Locate platelets.
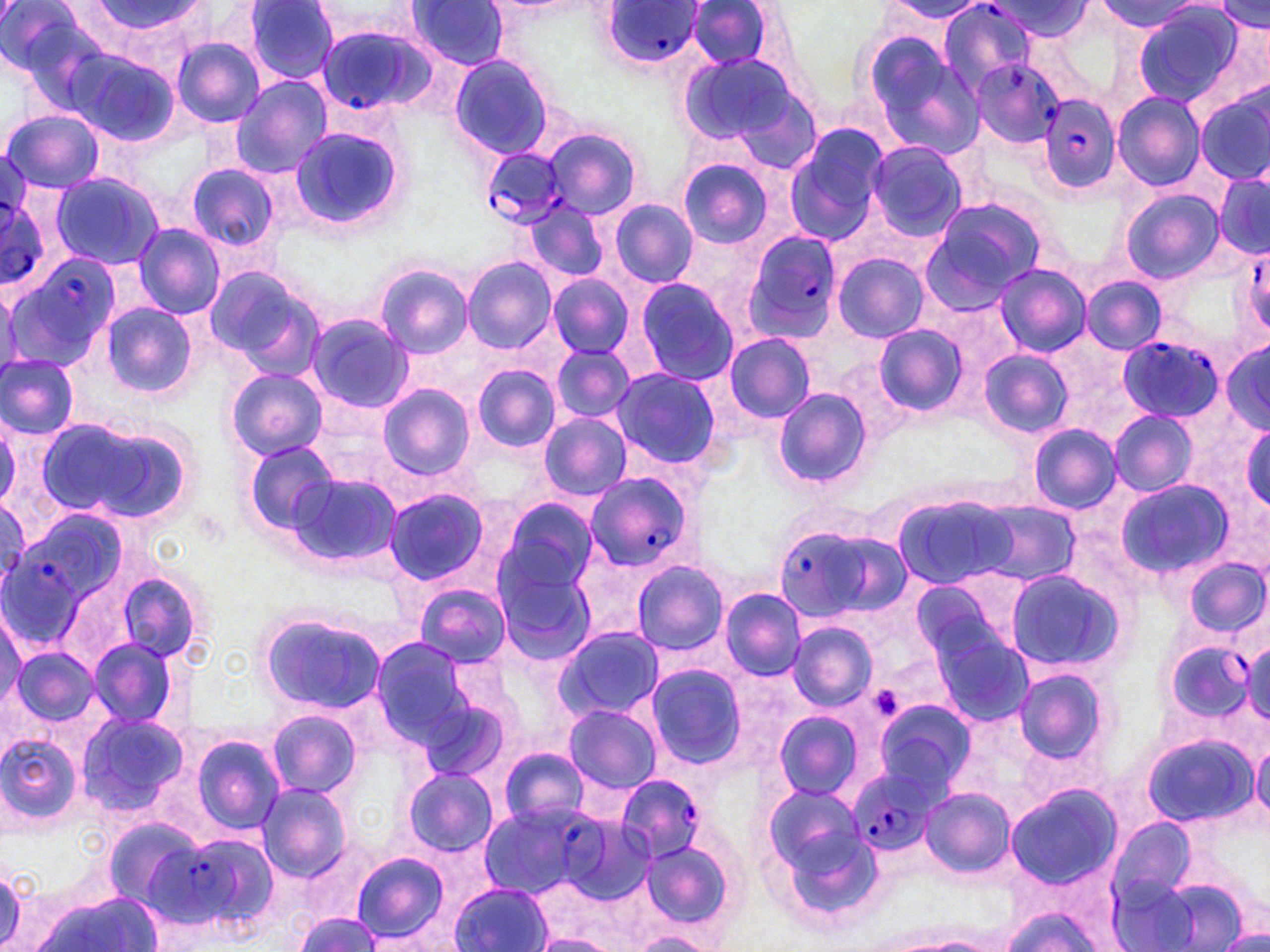

Approximate bounding boxes as (x1,y1)-(x2,y2) corner pairs in pixels.
Platelets: (868,683)-(907,723).

Summary:
  - Plasmodium falciparum-infected red blood cell locations (subset): (940,0)-(1040,91), (599,2)-(704,72), (311,15)-(430,114), (966,58)-(1062,148), (1036,92)-(1121,196), (479,148)-(568,231), (0,193)-(47,283), (740,229)-(846,343), (1251,251)-(1270,328), (7,255)-(124,374), (1117,338)-(1220,422), (583,470)-(699,574), (776,522)-(907,625), (0,536)-(83,646), (1166,636)-(1256,722), (851,768)-(937,857), (614,773)-(706,860), (156,830)-(280,937)
  - Uninfected red blood cell locations (subset): (89,0)-(204,42), (406,0)-(512,69), (1101,0)-(1201,32), (1,1)-(103,101), (243,1)-(340,84), (885,1)-(987,22), (686,2)-(773,70), (989,2)-(1088,41), (306,3)-(423,49), (1215,3)-(1268,34), (1132,5)-(1242,106), (862,35)-(985,157), (171,37)-(264,127), (63,47)-(180,146), (448,54)-(555,161), (679,54)-(806,153), (230,77)-(331,179), (1112,92)-(1206,192), (1197,93)-(1270,184), (2,109)-(104,193), (785,124)-(888,246), (287,126)-(404,232), (542,126)-(642,220), (867,141)-(965,241), (678,158)-(772,247), (185,162)-(279,253), (49,172)-(165,270), (1214,172)-(1270,258), (1120,188)-(1224,282), (918,197)-(1048,308), (609,199)-(699,287), (523,201)-(610,284), (133,225)-(224,319), (834,252)-(927,342), (462,256)-(558,355), (992,262)-(1089,358), (375,264)-(472,357), (201,266)-(319,375), (547,276)-(634,359), (1080,276)-(1167,356), (633,277)-(739,387), (100,304)-(197,399), (306,313)-(412,412), (872,324)-(968,415), (722,333)-(816,423), (1221,339)-(1270,434), (548,344)-(636,424), (979,348)-(1073,438), (0,355)-(78,439), (826,355)-(917,448), (471,364)-(562,452), (610,367)-(727,473), (227,368)-(328,460), (0,370)-(111,485), (377,383)-(476,480), (771,388)-(871,490), (1109,409)-(1198,496), (537,412)-(634,501), (0,413)-(21,511), (37,415)-(181,524), (1028,423)-(1119,513), (1242,423)-(1270,513), (242,439)-(339,533), (287,471)-(402,570), (1114,478)-(1232,579), (383,488)-(490,586), (895,494)-(1018,588), (498,499)-(599,598), (973,500)-(1080,585), (492,554)-(601,672), (1183,557)-(1269,636), (630,559)-(730,656), (1002,568)-(1126,675), (112,570)-(210,667), (909,571)-(1022,670), (413,581)-(509,668), (720,587)-(807,680), (256,608)-(388,715), (1,612)-(26,709), (788,622)-(876,712), (930,625)-(1035,729), (555,627)-(666,722), (370,636)-(477,747), (88,638)-(180,729), (1247,640)-(1270,726), (11,646)-(99,727), (645,663)-(748,769), (1012,665)-(1112,768), (417,696)-(509,788), (872,698)-(975,795), (564,704)-(661,794), (266,708)-(360,799), (773,709)-(864,801), (76,711)-(191,821), (0,731)-(84,832), (190,733)-(285,833), (1141,734)-(1258,828), (1252,741)-(1270,826), (499,747)-(589,829), (402,767)-(498,858), (758,781)-(875,898), (255,784)-(352,882), (1004,785)-(1122,888), (920,788)-(1015,879), (564,816)-(660,904), (100,817)-(205,910), (1106,818)-(1199,922), (640,839)-(734,932), (351,852)-(450,944), (0,865)-(27,948), (452,882)-(551,952), (36,892)-(165,952), (290,906)-(387,952), (1002,908)-(1100,952), (633,932)-(710,951), (534,934)-(616,952), (863,934)-(992,952)
  - Slide-level diagnosis: Plasmodium falciparum
  - Field of view: one of a larger specimen
  - Magnification: 1000x
  - Modality: optical microscopy
  - Image size: 1270×952 pixels
  - Preparation: thin blood smear
  - Stain: May-Grünwald-Giemsa